Classify this cell by malaria status.
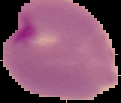
It is parasitized.

Summary:
  - Preparation: thin blood film
  - Image size: 121×103 pixels
  - Image type: cell region segmented out of the field of view; surrounding area masked to black